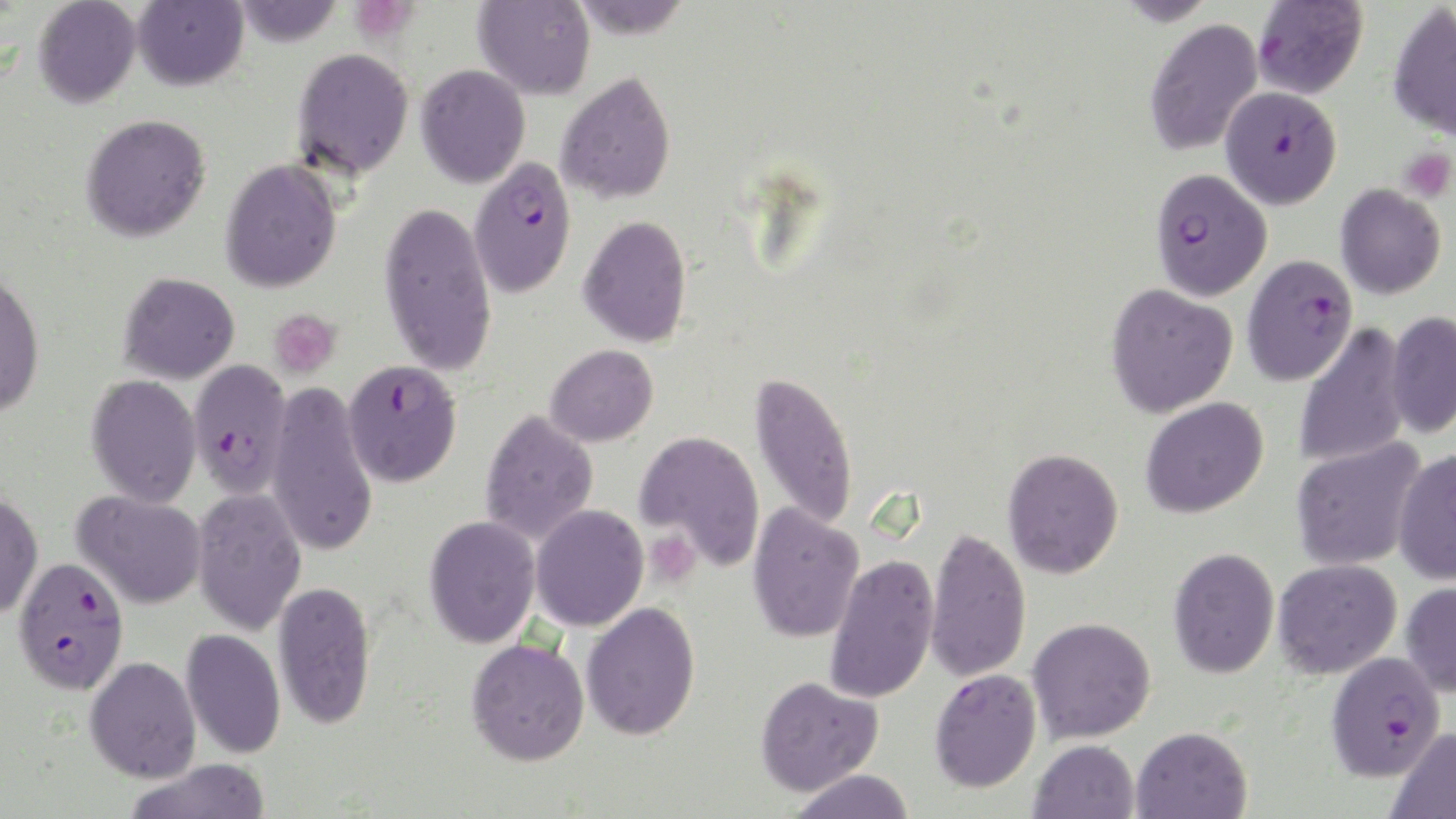 Approximate bounding boxes as [x1, y1, x2, y2] in pixels. Uninfected red blood cell locations: [33, 0, 141, 108], [231, 0, 345, 46], [132, 1, 248, 91], [473, 1, 596, 100], [1387, 2, 1456, 142], [1143, 18, 1263, 155], [292, 48, 414, 179], [415, 64, 531, 188], [556, 71, 677, 205], [80, 113, 211, 242], [220, 158, 342, 293], [1334, 183, 1446, 299], [379, 199, 497, 377], [578, 215, 692, 348], [0, 268, 46, 419], [118, 272, 240, 384], [1105, 283, 1238, 417], [1385, 311, 1456, 440], [1293, 324, 1411, 469], [545, 344, 658, 446], [749, 370, 859, 530], [86, 374, 202, 508], [266, 382, 378, 557], [1139, 397, 1269, 518], [479, 410, 599, 546], [635, 429, 765, 570], [1291, 437, 1427, 572], [1392, 446, 1456, 582], [1002, 448, 1123, 578], [192, 486, 307, 636], [0, 490, 44, 621], [73, 490, 207, 609], [747, 502, 864, 643], [530, 505, 648, 632], [424, 515, 541, 648], [925, 526, 1032, 683], [1168, 547, 1280, 678], [825, 553, 939, 704], [1273, 558, 1401, 679], [273, 579, 377, 730], [1400, 580, 1456, 697], [581, 602, 701, 740], [1027, 616, 1156, 743], [180, 628, 286, 759], [466, 638, 589, 765], [84, 655, 201, 782], [929, 669, 1042, 793], [755, 675, 884, 796], [1131, 726, 1253, 819], [1387, 726, 1456, 818], [1029, 739, 1140, 819], [126, 758, 272, 818], [788, 768, 916, 819]. Platelet locations: [357, 0, 418, 42], [1399, 147, 1455, 203], [268, 309, 341, 380], [644, 528, 702, 587]. Plasmodium falciparum-infected red blood cell locations: [1252, 1, 1368, 100], [1221, 86, 1341, 208], [468, 158, 577, 297], [1150, 168, 1273, 300], [1242, 254, 1358, 386], [343, 358, 462, 487], [188, 359, 291, 499], [12, 557, 130, 694], [1325, 649, 1446, 782]. Slide-level diagnosis: Plasmodium falciparum. Optical microscopy. 1000x magnification. May-Grünwald-Giemsa stain. Single field of view. Thin blood smear. Image is 1456×819 pixels.